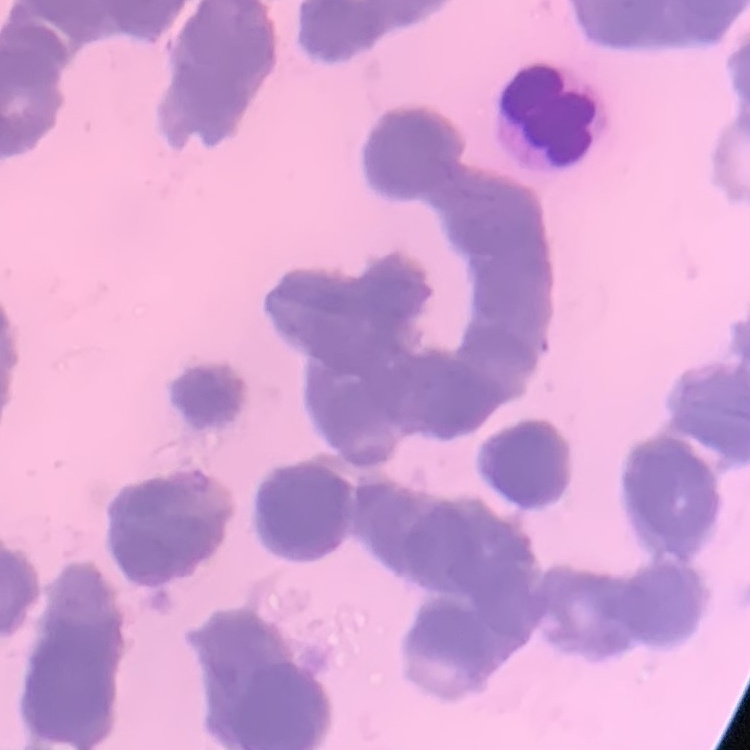

Summary:
  - Red blood cell morphology: rouleaux formation
  - Image type: one tile cut from a larger photomicrograph
  - Stain: Field's or Giemsa
  - Preparation: thin blood smear